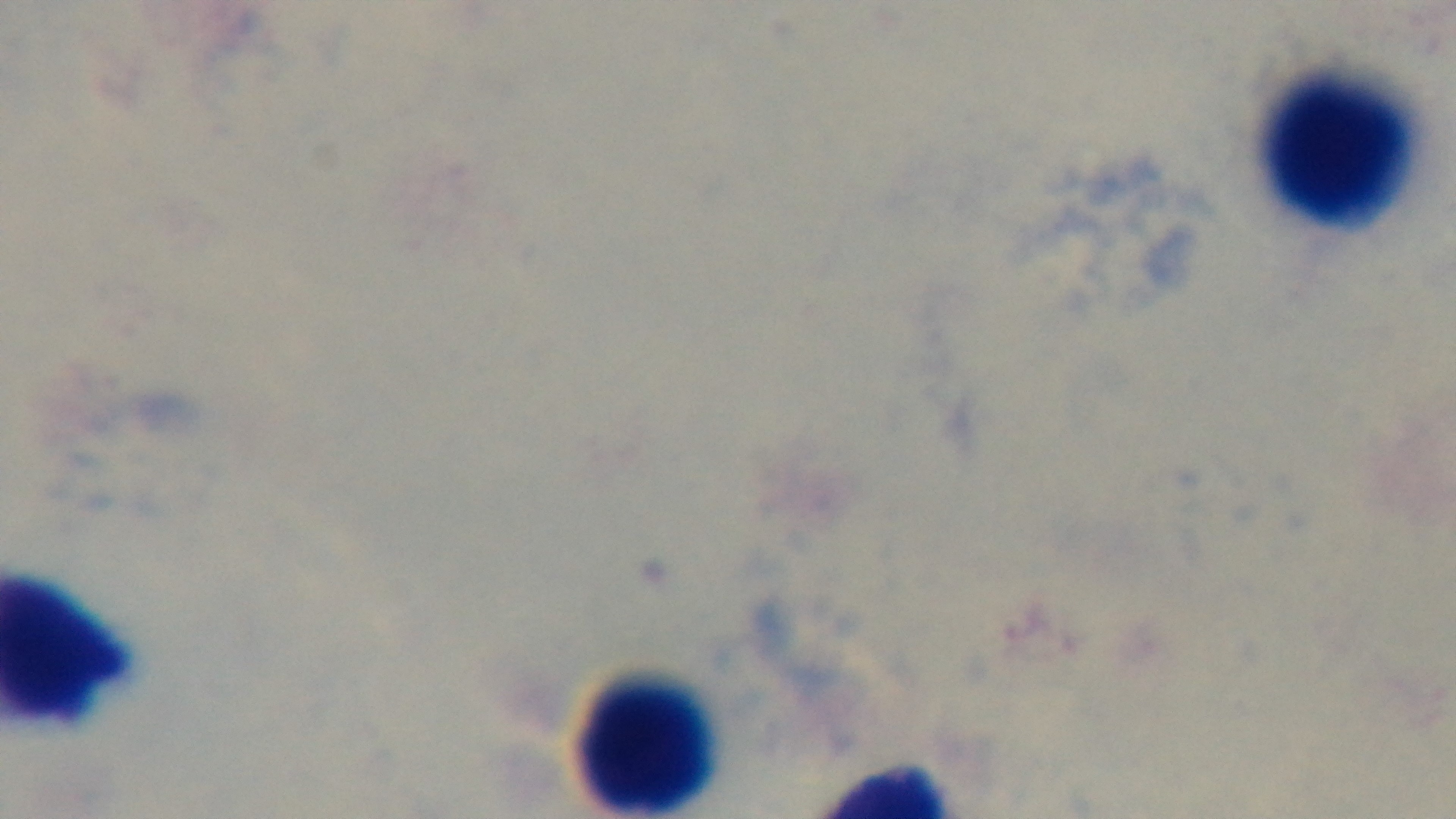 Malaria status: negative. Oil-immersion objective, 100x. Mounted 4K digital camera. One field from the slide. Giemsa-stained. Photomicrograph. Preparation: thick.